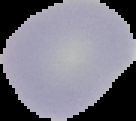
image size = 136×121 pixels
preparation = thin blood film
image type = segmented cell region on a black background
malaria status = uninfected